Draw a bounding box around every malaria parasite.
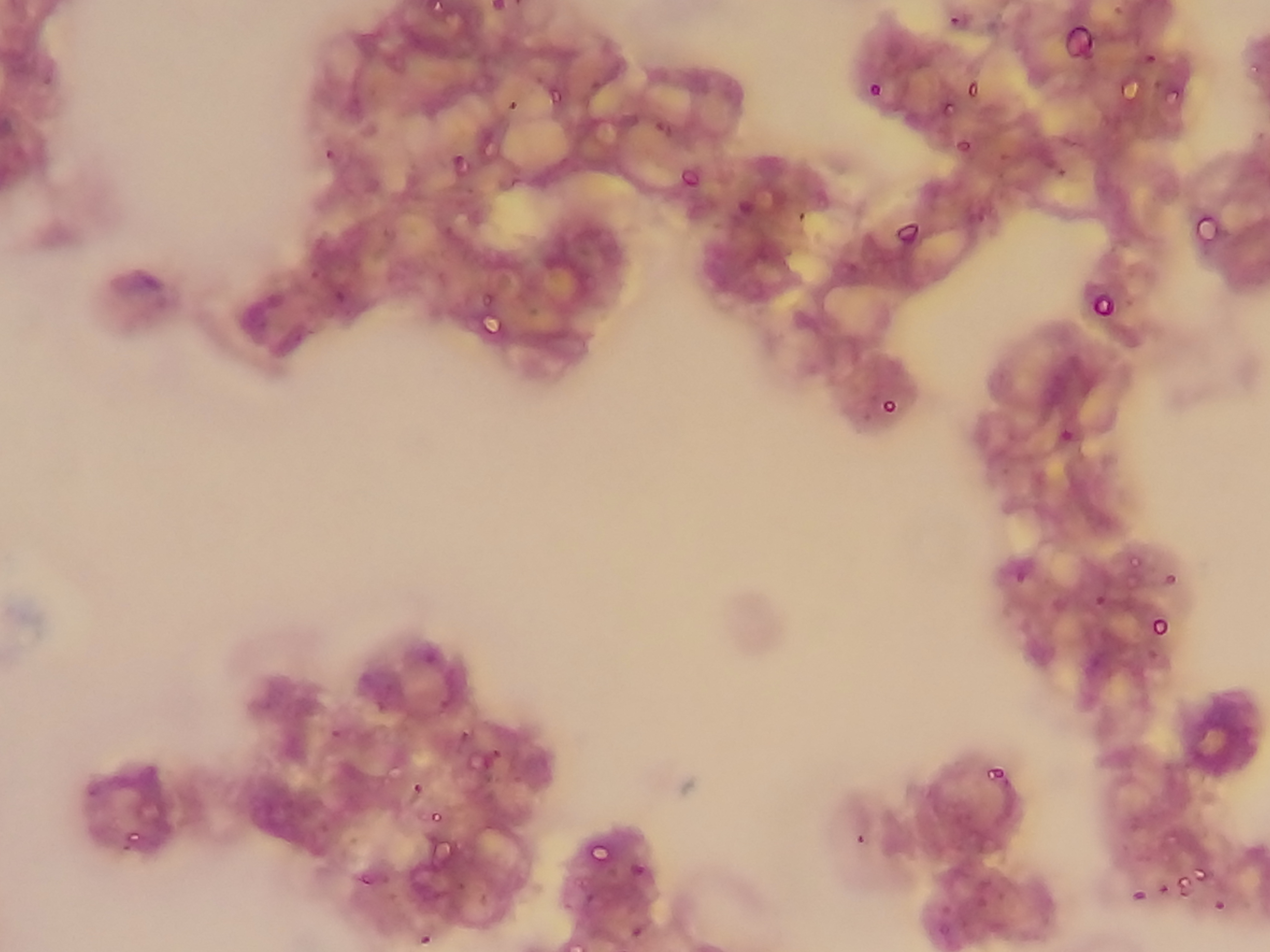

Approximate bounding boxes as (left, top, right, bottom) in pixels.
Malaria parasites: (429, 0, 445, 14), (490, 0, 509, 13), (509, 0, 525, 7), (948, 14, 961, 27), (1061, 21, 1096, 59), (1139, 50, 1157, 65), (1246, 51, 1264, 77), (530, 74, 546, 86), (588, 78, 603, 92), (1123, 78, 1141, 103), (867, 81, 884, 99), (965, 82, 980, 99), (1169, 83, 1186, 103), (549, 84, 568, 107), (507, 98, 519, 112), (942, 102, 955, 115), (651, 120, 669, 140), (954, 137, 971, 154), (322, 147, 336, 163), (997, 152, 1009, 164), (452, 153, 466, 169), (678, 164, 701, 187), (1055, 165, 1075, 179), (734, 192, 764, 217), (795, 209, 807, 223), (1191, 211, 1221, 242), (972, 216, 989, 226), (893, 218, 921, 246), (440, 224, 455, 237), (379, 225, 393, 240), (842, 258, 858, 270), (310, 269, 321, 282), (480, 285, 498, 311), (334, 287, 355, 304), (1088, 291, 1114, 317), (478, 310, 505, 335), (880, 396, 899, 416), (1055, 429, 1074, 445), (1127, 554, 1143, 571), (1009, 564, 1028, 582), (1162, 573, 1180, 585), (1094, 593, 1108, 608), (1150, 615, 1171, 637), (1144, 650, 1158, 660), (422, 651, 432, 668), (1080, 660, 1095, 669), (434, 697, 458, 709), (374, 701, 386, 714), (330, 728, 341, 740), (459, 728, 473, 743), (487, 743, 504, 757), (467, 749, 491, 770), (142, 759, 157, 775), (383, 762, 405, 783), (987, 765, 1005, 783), (411, 782, 423, 795), (83, 784, 99, 797), (428, 810, 444, 824), (123, 827, 143, 850), (853, 831, 867, 847), (1162, 834, 1180, 847), (426, 839, 449, 861), (586, 840, 610, 863), (454, 842, 464, 855), (630, 861, 649, 877), (1193, 867, 1209, 883), (356, 871, 373, 888), (974, 875, 992, 893), (1174, 877, 1190, 896), (1128, 878, 1147, 900), (1157, 882, 1171, 896), (477, 890, 490, 905), (582, 892, 595, 904), (975, 897, 987, 910), (1212, 898, 1226, 913), (938, 901, 956, 915), (629, 923, 645, 941), (932, 923, 946, 939), (417, 930, 433, 948), (565, 941, 579, 952).

Sample from Ghana. Thin blood film. Mobile-phone photograph taken through the microscope. Image is 1270×952 pixels. One field of view.